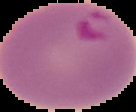
Summary:
  - Malaria status: parasitized
  - Preparation: thin blood smear
  - Image type: segmented cell region on a black background
  - Image size: 136×112 pixels